Report the malaria status of this cell.
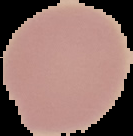

Uninfected.

The area outside the segmented cell region is set to black. From a thin blood smear. Image is 133×136 pixels.